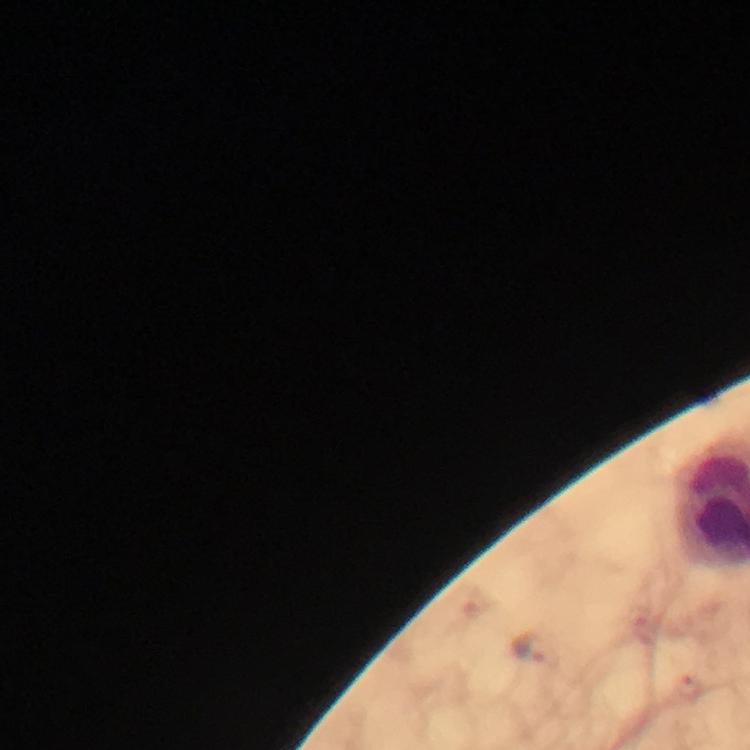
Approximate centers as (x, y) in pixels.
Summary:
  - Plasmodium parasite locations: (532, 649)
  - Stain: Giemsa
  - Image size: 750×750 pixels
  - Capture: smartphone camera through the microscope
  - Immersion oil: used
  - Magnification: 100x
  - Cropped from: one field of view
  - Context: from a malaria diagnostic workup
  - Preparation: thick smear